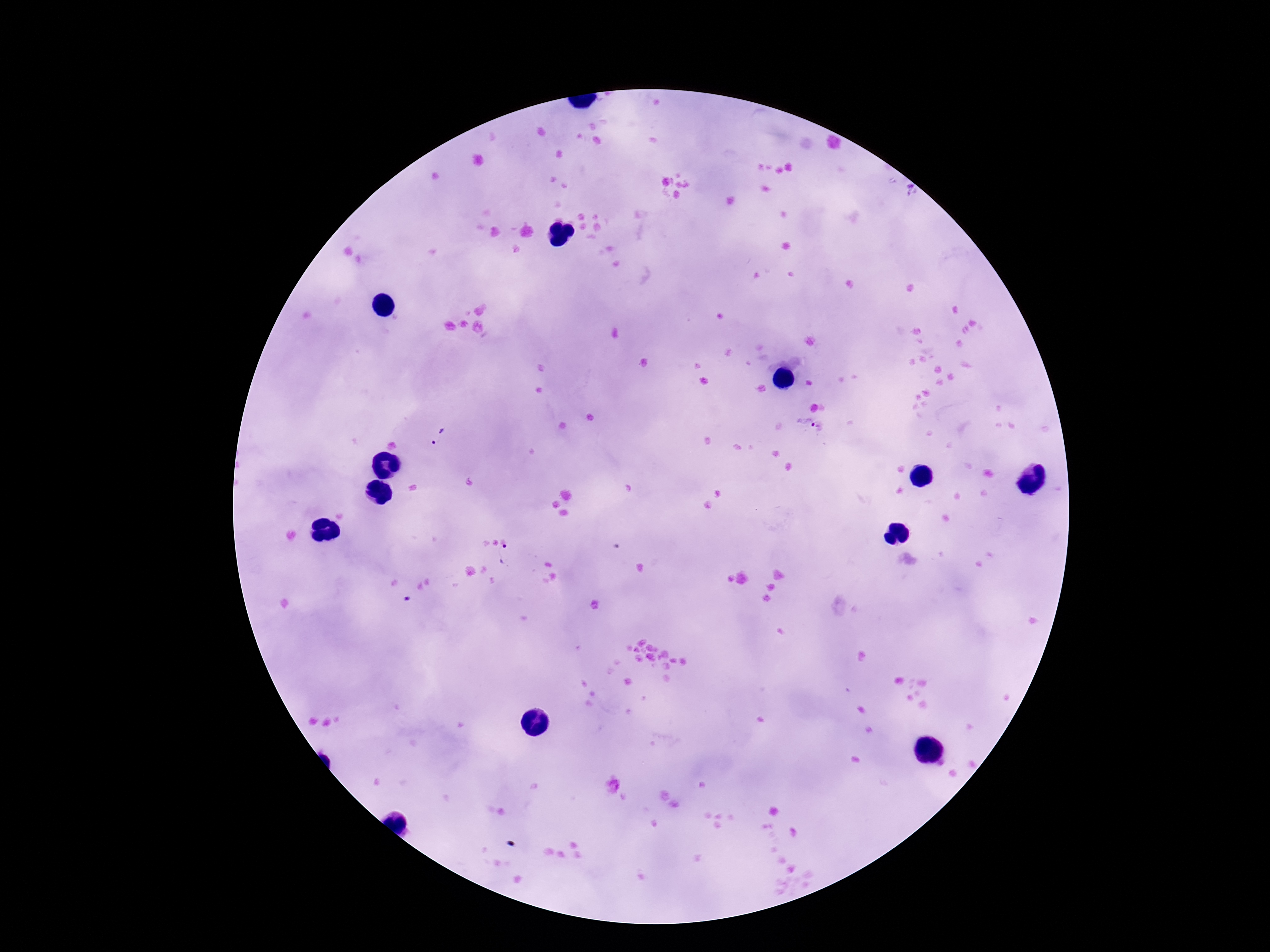
patient malaria status = positive
Plasmodium parasite locations = approximate centers as {x, y} in pixels: {911, 190}, {810, 428}, {438, 437}, {505, 554}, {408, 599}
capture = smartphone camera through the microscope eyepiece
image size = 1270×952 pixels
preparation = thick blood smear
magnification = 100x
stain = Giemsa
field of view = one from this slide